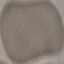

Result: negative for malaria parasites. Automatically extracted cell patch, resized to 64 × 64 pixels. Thin smear of blood. Acquired by smartphone through the microscope eyepiece. Giemsa stain.